Name the cell type shown.
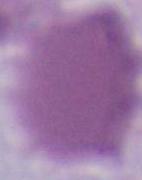
An erythrocyte.

Summary:
  - Modality: micrograph
  - Magnification: 1000x